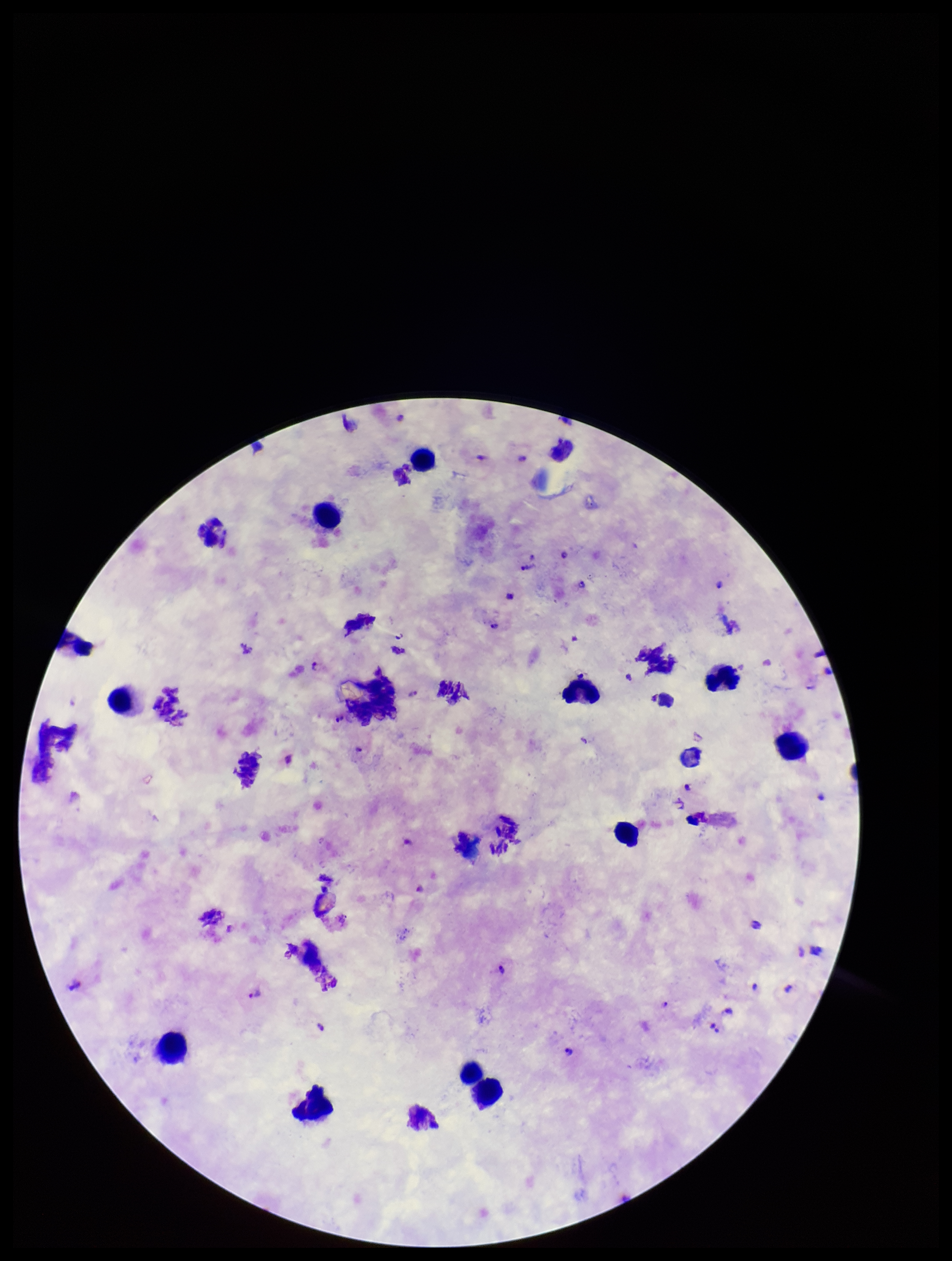

Plasmodium parasites = identified
patient malaria status = infected
field of view = single
species reported for this patient = Plasmodium falciparum
preparation = thick smear
stain = Giemsa
image size = 952×1261 pixels
parasite count = 15
leukocyte count = 13
capture = smartphone photograph through the microscope eyepiece